State which parasite is depicted.
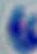

Toxoplasma gondii.

Captured at 1000x magnification. Photomicrograph.